Identify the blood parasite species.
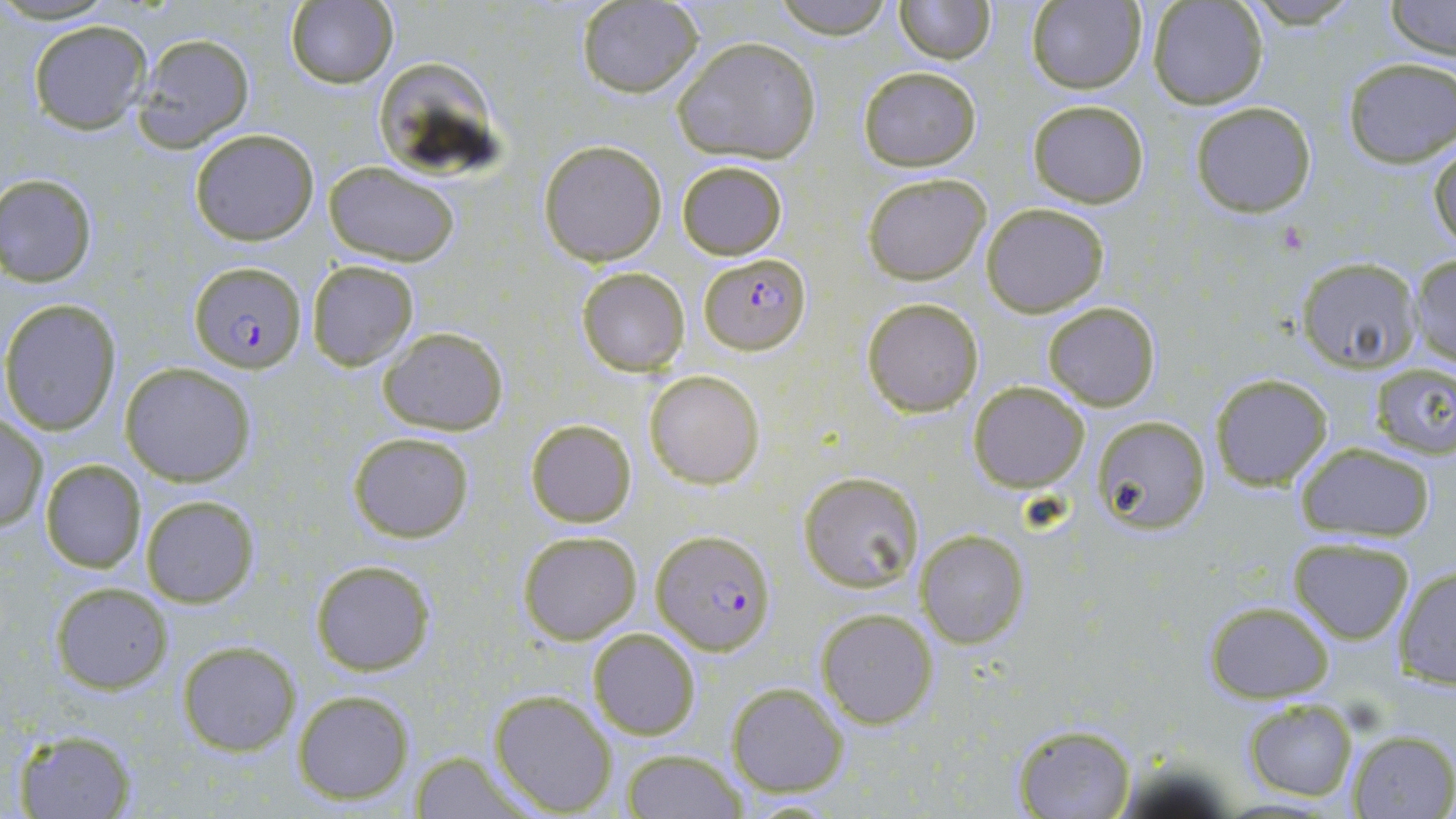

Plasmodium falciparum.

Summary:
  - Coordinate format: approximate bounding boxes as (x1,y1)-(x2,y2) corner pairs in pixels
  - Uninfected red blood cell locations: (770,0)-(898,37), (893,0)-(994,64), (1025,1)-(1148,95), (1147,1)-(1270,110), (1386,1)-(1454,61), (283,2)-(398,88), (575,2)-(703,98), (26,20)-(152,134), (133,32)-(256,151), (673,37)-(821,164), (1341,57)-(1456,168), (377,61)-(500,180), (857,65)-(981,171), (1025,98)-(1150,206), (1190,100)-(1316,218), (189,129)-(318,244), (1430,138)-(1455,254), (538,139)-(668,265), (676,160)-(787,259), (323,162)-(461,267), (1,172)-(99,285), (861,172)-(992,284), (981,202)-(1109,316), (1407,253)-(1456,369), (1297,258)-(1421,372), (305,259)-(420,369), (576,266)-(689,376), (861,298)-(982,416), (2,299)-(121,434), (1041,301)-(1161,409), (377,325)-(510,437), (120,362)-(256,487), (1370,362)-(1456,458), (643,368)-(765,490), (1209,374)-(1332,491), (967,382)-(1090,492), (0,415)-(48,532), (1091,416)-(1211,533), (525,419)-(637,528), (348,431)-(475,543), (1297,442)-(1435,542), (40,459)-(146,573), (799,472)-(922,593), (140,494)-(260,608), (516,530)-(641,644), (916,531)-(1029,647), (1287,537)-(1416,643), (310,560)-(434,676), (1392,564)-(1456,689), (49,581)-(172,692), (1202,600)-(1337,702), (815,607)-(940,729), (588,627)-(702,741), (177,640)-(301,755), (546,641)-(672,774), (726,682)-(848,798), (291,688)-(415,805), (489,690)-(617,814), (1242,699)-(1357,801), (1010,722)-(1135,818), (12,727)-(140,818), (1348,730)-(1456,817), (622,749)-(746,818), (409,751)-(533,817)
  - Plasmodium falciparum-infected red blood cell locations: (701,254)-(811,354), (188,263)-(305,372), (652,529)-(776,653)
  - Magnification: 1000x
  - Field of view: single
  - Stain: May-Grünwald-Giemsa
  - Image size: 1456×819 pixels
  - Modality: optical microscopy
  - Preparation: thin blood smear